Classify this cell by malaria status.
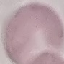
Uninfected.

Summary:
  - Capture: smartphone camera at the microscope eyepiece
  - Image type: cell patch, automatically extracted from a larger field of view and resized to 64 × 64 pixels
  - Preparation: thin smear
  - Stain: Giemsa